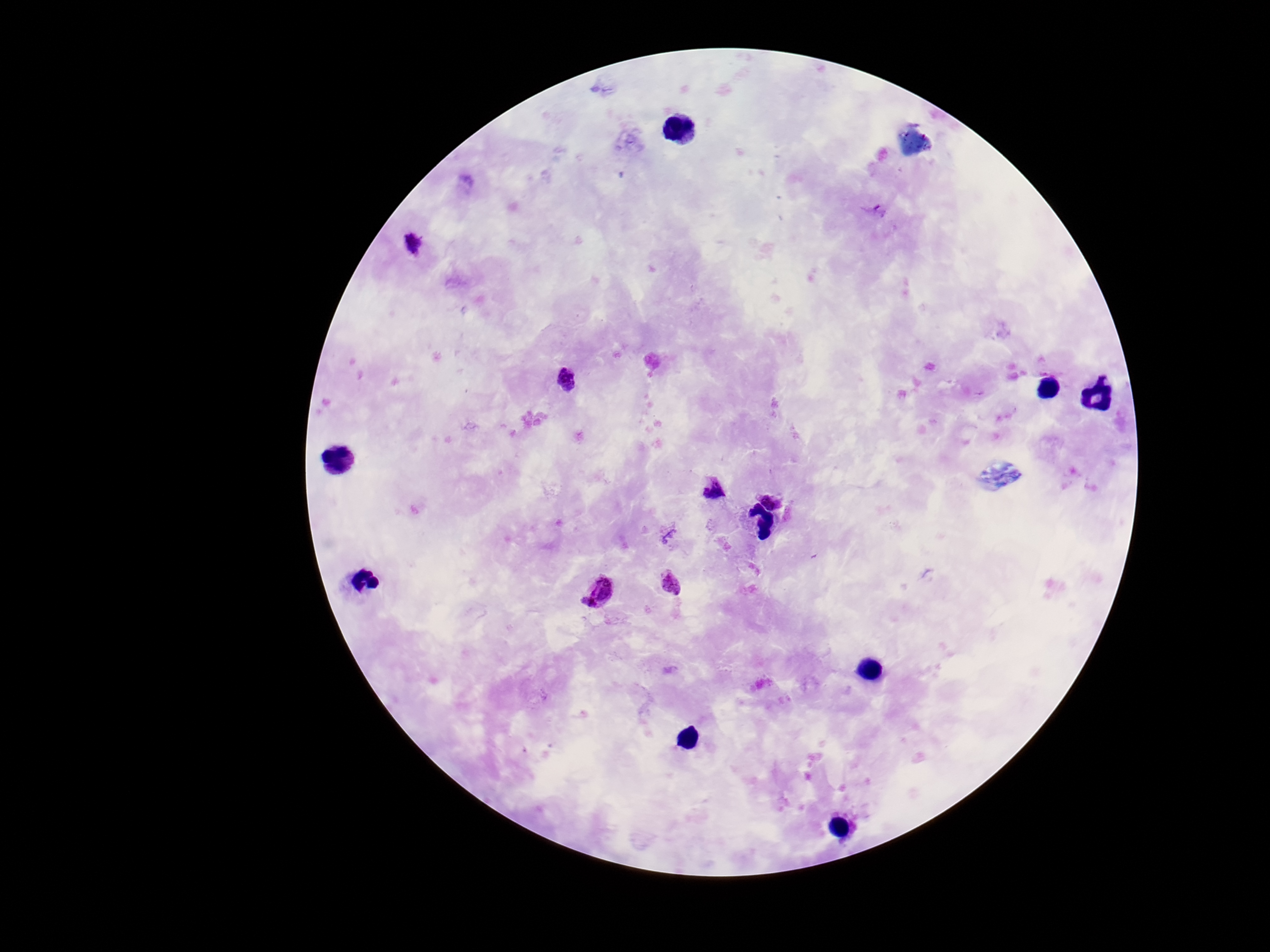
Approximate centers as {x, y} in pixels. Plasmodium parasite locations: {877, 212}, {414, 243}, {570, 382}, {713, 489}, {772, 499}, {671, 583}, {600, 590}. Patient malaria status: positive. Giemsa stain. Image is 1270×952 pixels. Thick peripheral-blood smear. Photographed through the microscope eyepiece with a smartphone camera. Single field of view. 100x magnification.